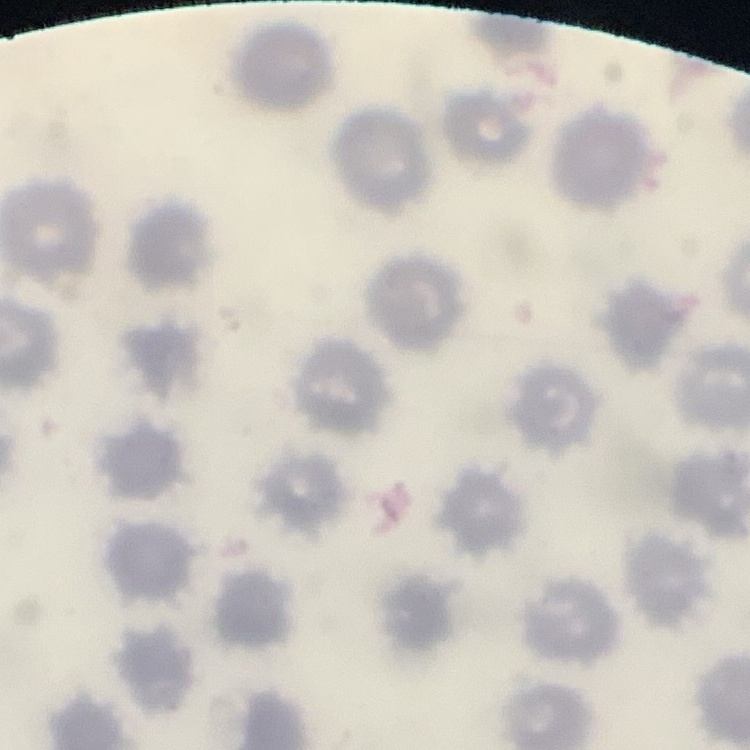

The erythrocytes exhibit no rouleaux formation. Thin blood smear. Stained with either Field's or Giemsa. Square crop of a larger photomicrograph.